Assess this cell for malaria.
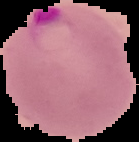
It is parasitized.

Summary:
  - Image size: 139×142 pixels
  - Image type: segmented cell region with the area outside set to black
  - Preparation: thin blood film